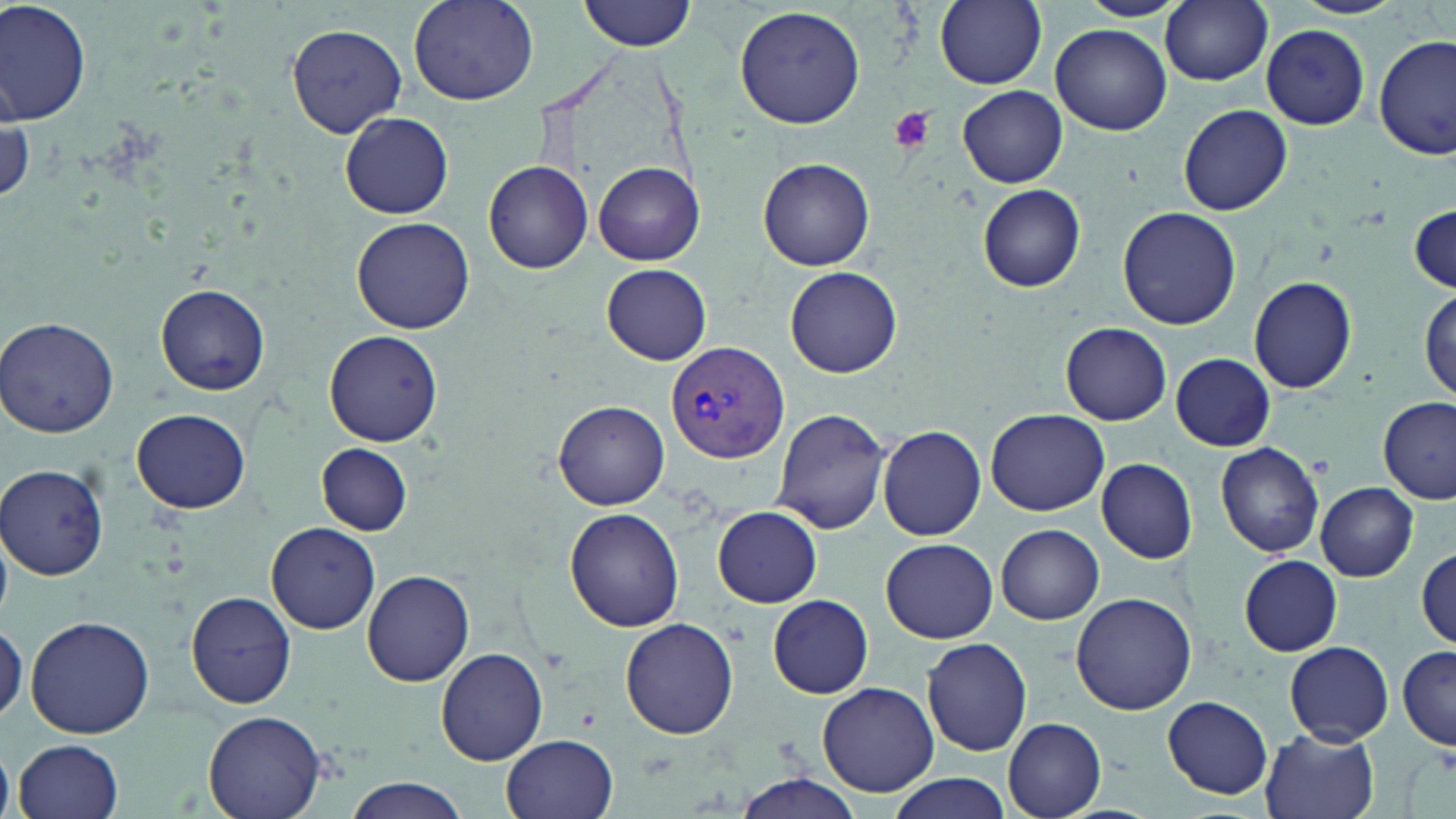
slide-level diagnosis = Plasmodium vivax
uninfected red blood cell locations = approximate bounding boxes as named x1/y1/x2/y2 corners in pixels: (x1=1, y1=0, x2=93, y2=128), (x1=408, y1=0, x2=538, y2=107), (x1=578, y1=0, x2=695, y2=53), (x1=933, y1=0, x2=1046, y2=89), (x1=1077, y1=0, x2=1188, y2=21), (x1=1161, y1=0, x2=1274, y2=86), (x1=1294, y1=0, x2=1406, y2=19), (x1=734, y1=5, x2=867, y2=131), (x1=287, y1=24, x2=408, y2=136), (x1=1051, y1=24, x2=1170, y2=135), (x1=1262, y1=24, x2=1371, y2=129), (x1=1375, y1=34, x2=1454, y2=159), (x1=957, y1=86, x2=1067, y2=187), (x1=1178, y1=105, x2=1291, y2=216), (x1=340, y1=112, x2=454, y2=220), (x1=758, y1=157, x2=875, y2=271), (x1=484, y1=160, x2=593, y2=274), (x1=594, y1=163, x2=703, y2=266), (x1=977, y1=184, x2=1086, y2=292), (x1=1410, y1=204, x2=1455, y2=294), (x1=1119, y1=208, x2=1241, y2=330), (x1=351, y1=215, x2=475, y2=333), (x1=601, y1=263, x2=712, y2=364), (x1=785, y1=266, x2=902, y2=379), (x1=1249, y1=275, x2=1357, y2=394), (x1=157, y1=283, x2=271, y2=394), (x1=1417, y1=288, x2=1454, y2=405), (x1=1, y1=316, x2=120, y2=438), (x1=1060, y1=322, x2=1171, y2=425), (x1=325, y1=328, x2=443, y2=447), (x1=1171, y1=353, x2=1275, y2=450), (x1=1376, y1=397, x2=1455, y2=503), (x1=554, y1=400, x2=670, y2=509), (x1=770, y1=407, x2=891, y2=534), (x1=985, y1=407, x2=1111, y2=515), (x1=132, y1=408, x2=252, y2=512), (x1=879, y1=426, x2=987, y2=540), (x1=1215, y1=442, x2=1325, y2=557), (x1=316, y1=444, x2=412, y2=534), (x1=1096, y1=457, x2=1199, y2=564), (x1=1, y1=464, x2=109, y2=578), (x1=1316, y1=482, x2=1418, y2=580), (x1=564, y1=506, x2=685, y2=632), (x1=712, y1=507, x2=824, y2=609), (x1=267, y1=523, x2=380, y2=634), (x1=996, y1=524, x2=1104, y2=624), (x1=880, y1=538, x2=997, y2=643), (x1=1416, y1=546, x2=1454, y2=649), (x1=1239, y1=555, x2=1342, y2=656), (x1=363, y1=571, x2=475, y2=686), (x1=187, y1=590, x2=297, y2=709), (x1=1070, y1=592, x2=1195, y2=716), (x1=769, y1=595, x2=873, y2=698), (x1=26, y1=615, x2=155, y2=738), (x1=621, y1=617, x2=739, y2=739), (x1=0, y1=622, x2=27, y2=724), (x1=920, y1=637, x2=1032, y2=756), (x1=1284, y1=642, x2=1393, y2=744), (x1=1399, y1=643, x2=1456, y2=750), (x1=435, y1=646, x2=550, y2=766), (x1=816, y1=681, x2=942, y2=798), (x1=1161, y1=695, x2=1273, y2=798), (x1=203, y1=709, x2=326, y2=819), (x1=1003, y1=718, x2=1106, y2=817), (x1=1259, y1=723, x2=1381, y2=819), (x1=501, y1=734, x2=618, y2=819), (x1=15, y1=739, x2=124, y2=819), (x1=883, y1=772, x2=1013, y2=818), (x1=734, y1=774, x2=863, y2=818), (x1=346, y1=777, x2=470, y2=819)
stain = May-Grünwald-Giemsa
field of view = one of a larger specimen
Plasmodium vivax-infected red blood cell locations = approximate bounding boxes as named x1/y1/x2/y2 corners in pixels: (x1=665, y1=339, x2=788, y2=466)
modality = optical microscopy
image size = 1456×819 pixels
magnification = 1000x
preparation = thin blood smear
platelet locations = approximate bounding boxes as named x1/y1/x2/y2 corners in pixels: (x1=888, y1=106, x2=936, y2=154), (x1=1437, y1=745, x2=1456, y2=776)